Describe the morphology of the erythrocytes.
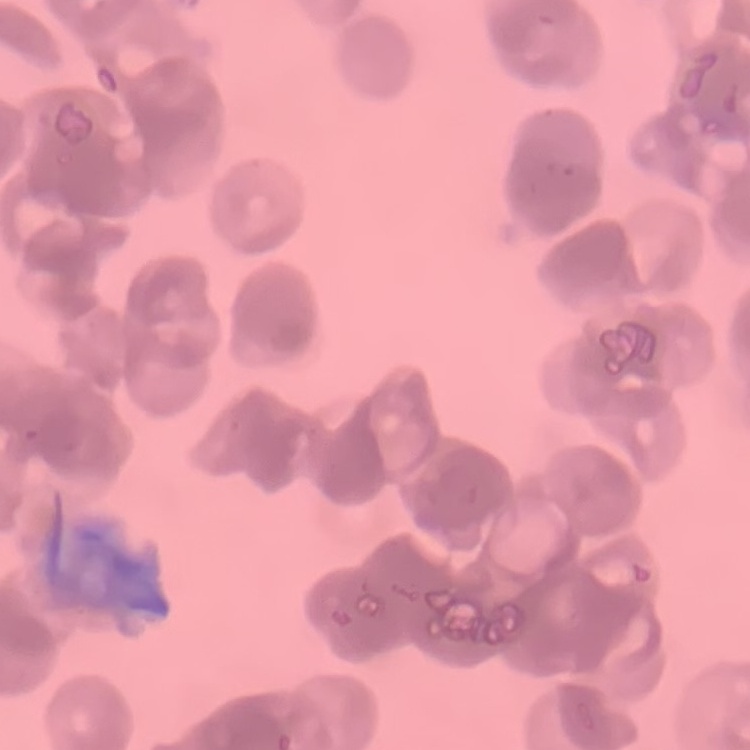

Rouleaux formation.

Summary:
  - Image type: square crop of a larger photomicrograph
  - Preparation: thin peripheral smear
  - Stain: Field's or Giemsa